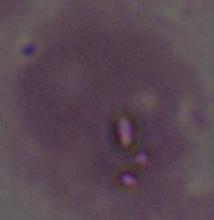

Summary:
  - Modality: micrograph
  - Identification: erythrocyte
  - Magnification: 1000x